State the preparation type.
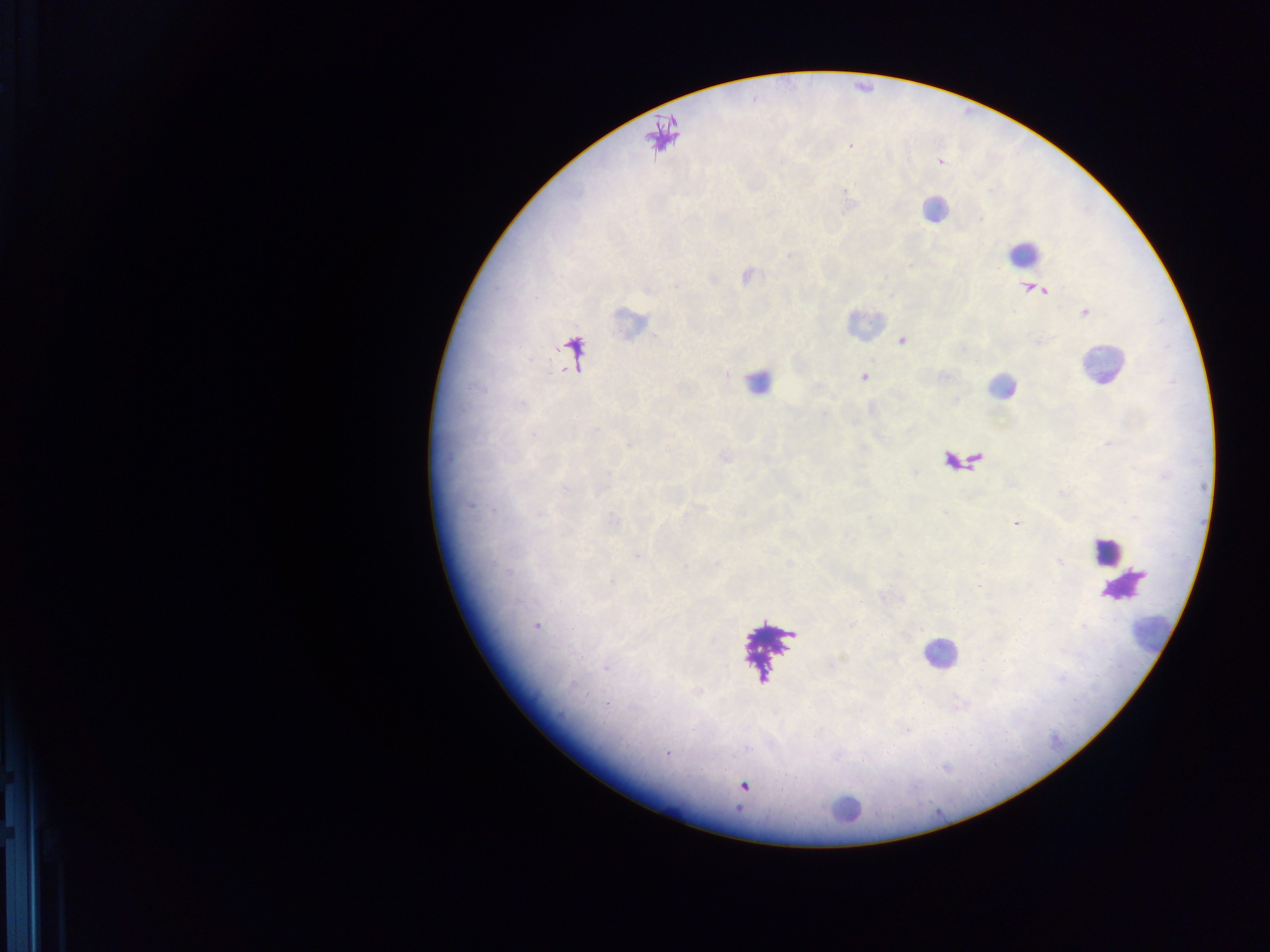

This is a thick smear.

Approximate centers as (x, y) in pixels.
Summary:
  - Leukocyte locations (subset; some below the resolvable size): (933, 210), (1023, 252), (627, 321), (863, 321), (1100, 365), (757, 381), (1000, 387), (1107, 550), (1123, 586), (1153, 631), (939, 654), (843, 809)
  - Malaria parasite locations: (902, 341), (864, 377), (534, 434), (628, 444), (470, 506), (1016, 524), (637, 557), (1059, 561), (536, 627), (605, 668), (607, 704), (666, 753), (743, 787)
  - Field of view: single
  - Capture: mobile-phone photograph through a microscope
  - Image size: 1270×952 pixels
  - Country: Ghana